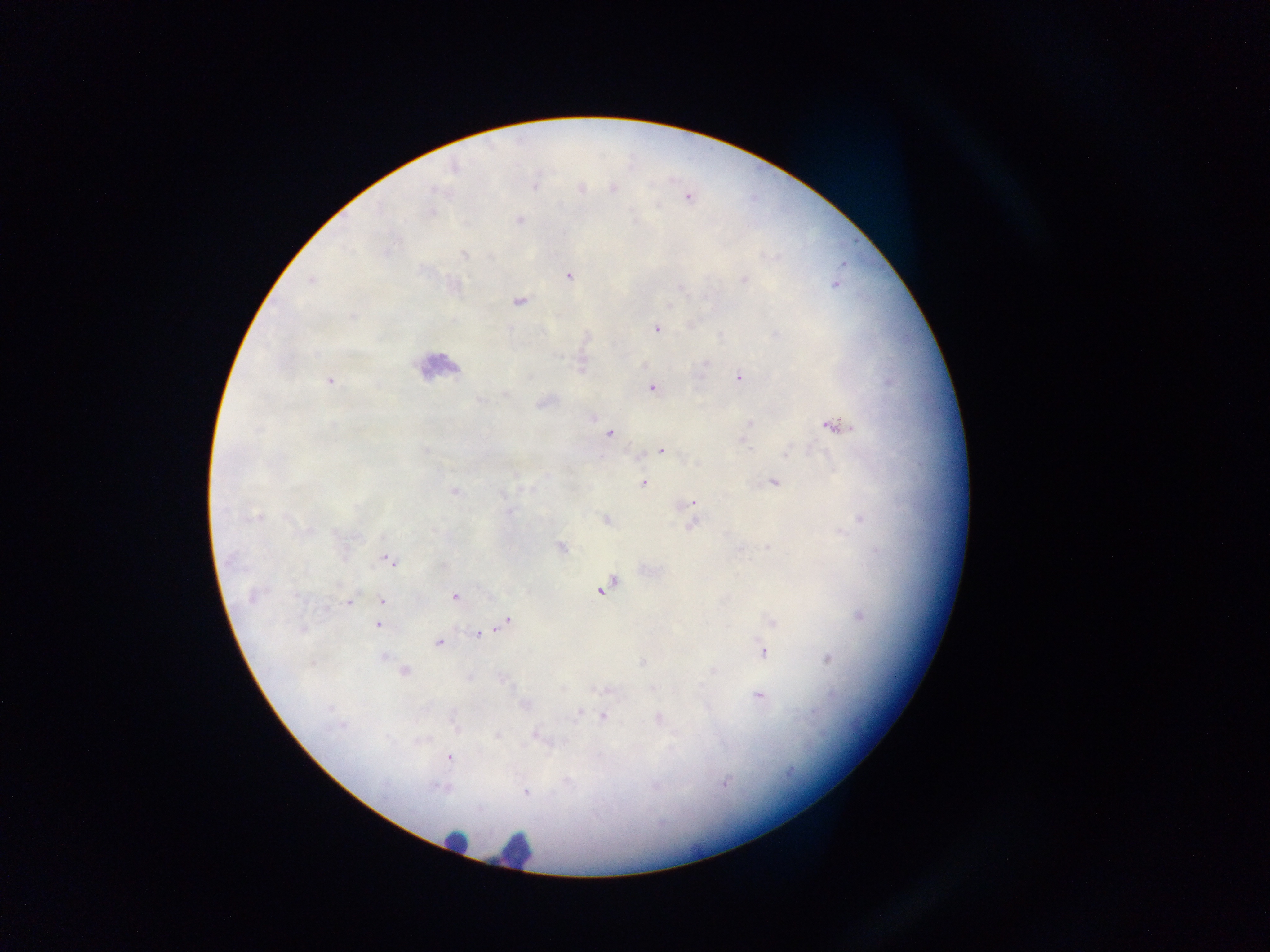

country = Ghana
leukocyte locations = approximate centers as [x, y] in pixels: [437, 366], [456, 841], [514, 849]
image size = 1270×952 pixels
field of view = single
preparation = thick blood film
capture = mobile-phone photograph through a microscope
Plasmodium parasite locations = approximate centers as [x, y] in pixels: [535, 184], [613, 188], [580, 189], [687, 196], [430, 212], [519, 220], [568, 275], [312, 280], [836, 283], [518, 301], [656, 327], [582, 365], [739, 376], [328, 381], [651, 387], [544, 402], [592, 417], [833, 424], [749, 425], [609, 433], [743, 439], [662, 450], [644, 482], [773, 482], [455, 491], [693, 502], [692, 510], [606, 519], [692, 523], [560, 547], [387, 559], [604, 587], [252, 595], [454, 597], [349, 600], [382, 600], [860, 615], [772, 622], [505, 623], [379, 624], [480, 633], [440, 641], [763, 651], [383, 656], [828, 659], [403, 670], [606, 689], [758, 694], [580, 710], [604, 715], [658, 719], [538, 735], [448, 757], [526, 791]